Assess this cell for malaria.
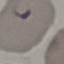
Parasitized.

Giemsa stain. Photographed with a smartphone camera at the microscope eyepiece. Cell patch, automatically extracted from a larger field of view and resized to 64 × 64 pixels. Thin smear of blood.